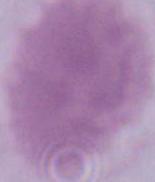
Captured at 1000x magnification. An erythrocyte is shown. Micrograph.